Assess this cell for malaria.
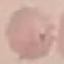

Uninfected.

Acquired by smartphone through the microscope eyepiece. Giemsa stain. Cell patch, automatically extracted from a larger field of view and resized to 64 × 64 pixels. Thin smear of blood.